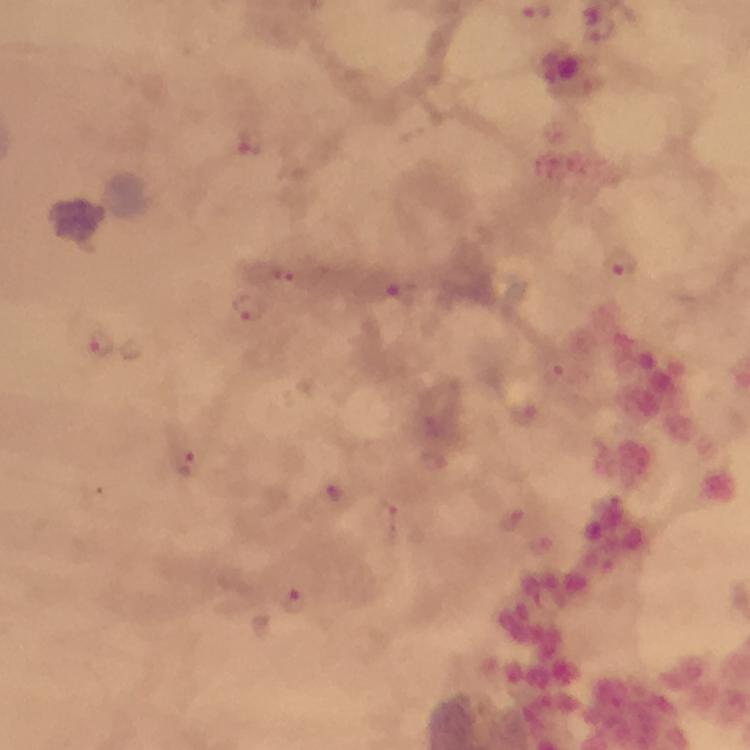 Approximate centers as (x, y) in pixels. Malaria parasite locations: (245, 147), (620, 266), (281, 274), (396, 300), (249, 310), (101, 346), (560, 370), (525, 414), (186, 463), (338, 493), (387, 521), (296, 602). Image is 750×750 pixels. Cropped region of a single field of view. From a malaria diagnostic workup. Photographed through the microscope with a smartphone camera. Immersion oil applied. Giemsa stain. At 100x magnification. Thick blood smear.